Name the blood parasite species.
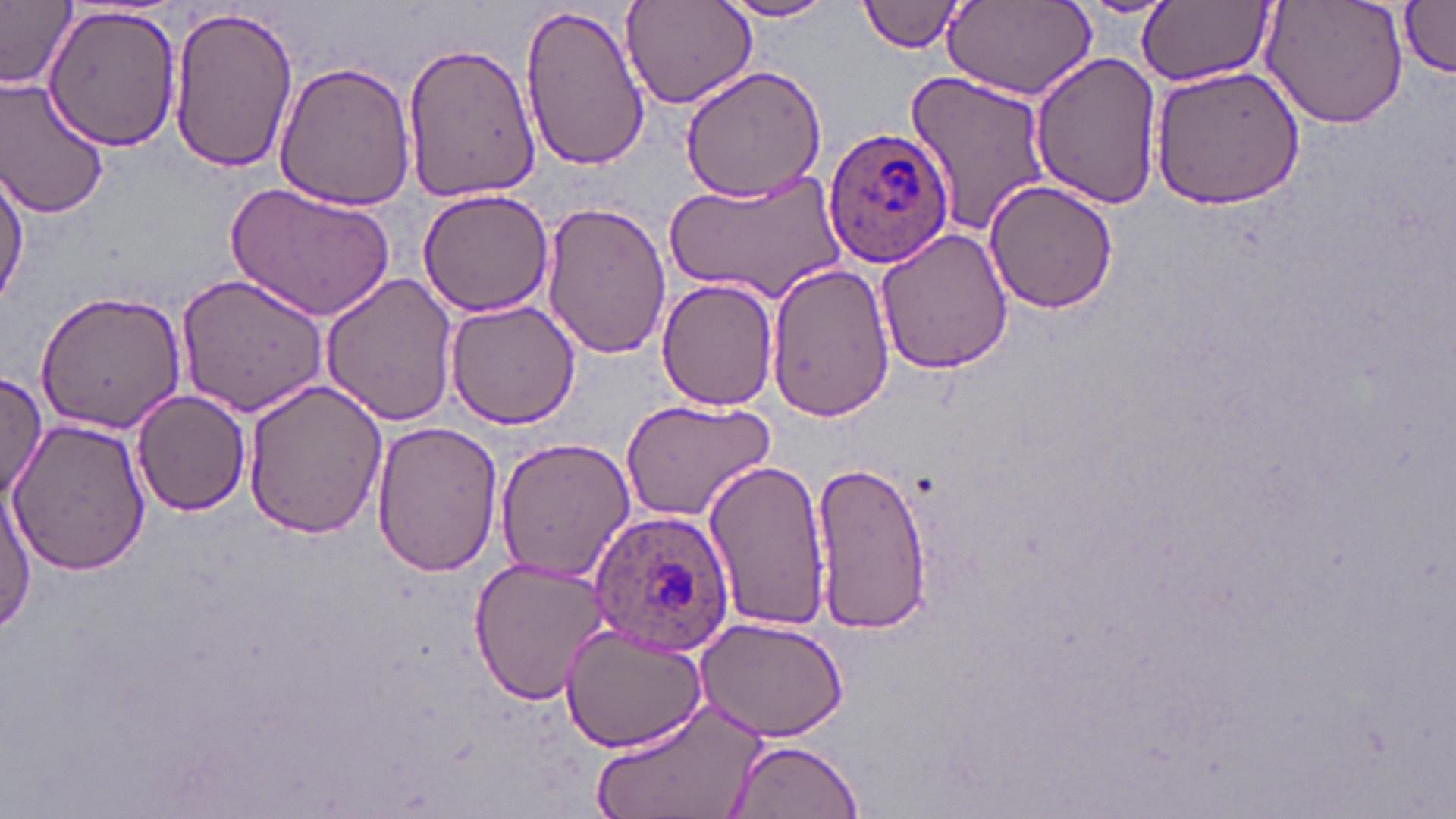

Plasmodium ovale.

magnification = 1000x
stain = May-Grünwald-Giemsa
preparation = thin blood smear
field of view = one of a larger specimen
image size = 1456×819 pixels
uninfected red blood cell locations = approximate bounding boxes as [x1, y1, x2, y2] in pixels: [618, 0, 756, 110], [717, 0, 839, 23], [858, 0, 970, 53], [1261, 0, 1407, 128], [40, 1, 184, 153], [0, 2, 77, 92], [520, 2, 649, 170], [944, 2, 1096, 101], [1140, 2, 1271, 86], [1400, 3, 1456, 77], [165, 7, 297, 173], [399, 38, 542, 204], [1029, 51, 1162, 208], [272, 61, 416, 212], [1151, 65, 1308, 208], [680, 67, 829, 202], [901, 69, 1053, 236], [0, 74, 112, 219], [1, 165, 28, 308], [669, 170, 845, 302], [985, 179, 1119, 315], [226, 181, 395, 322], [416, 187, 555, 318], [540, 200, 671, 359], [875, 228, 1013, 374], [765, 263, 896, 419], [321, 269, 460, 426], [176, 272, 333, 419], [656, 278, 779, 412], [34, 290, 187, 436], [445, 297, 584, 430], [0, 373, 48, 507], [243, 377, 389, 538], [132, 389, 251, 517], [618, 396, 777, 522], [7, 419, 151, 574], [371, 421, 502, 578], [494, 436, 638, 584], [702, 458, 833, 630], [808, 461, 931, 631], [0, 482, 37, 633], [468, 556, 610, 707], [693, 614, 849, 743], [559, 620, 707, 754], [595, 700, 767, 819], [725, 740, 864, 817]
modality = optical microscopy
Plasmodium ovale-infected red blood cell locations = approximate bounding boxes as [x1, y1, x2, y2] in pixels: [822, 124, 955, 269], [591, 510, 736, 656]